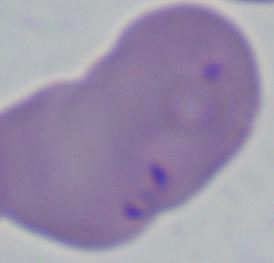

identification = Babesia
magnification = 1000x
modality = micrograph